Locate and identify every blood parasite.
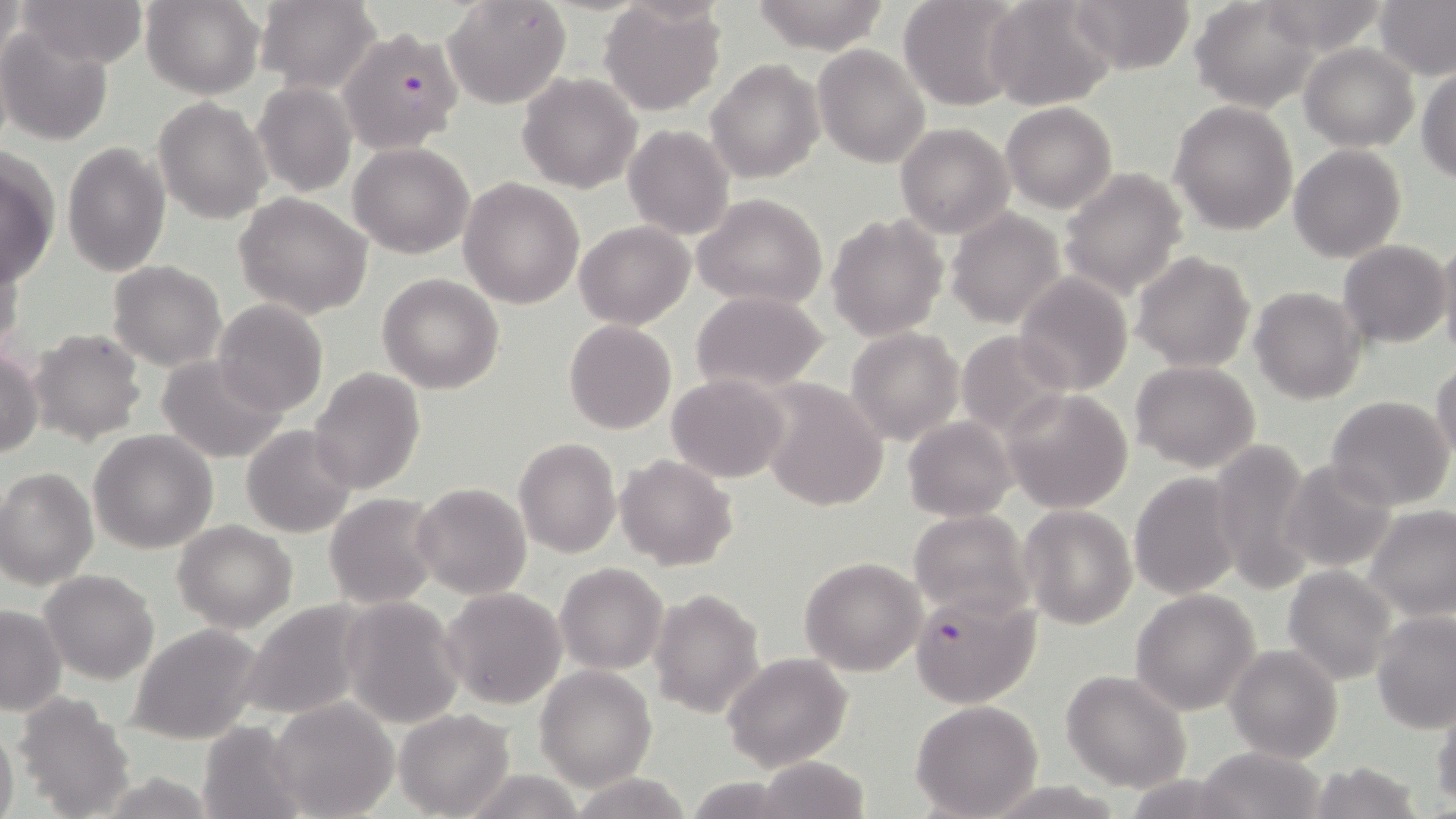

Approximate bounding boxes as (x1, y1, x2, y2) in pixels.
Plasmodium falciparum-infected red blood cells: (346, 25, 462, 150), (907, 589, 1042, 709).
No Plasmodium ovale, Plasmodium malariae, Plasmodium vivax, Babesia divergens, or Trypanosoma brucei observed.

Summary:
  - Uninfected red blood cell locations: (18, 0, 146, 67), (141, 0, 264, 98), (443, 0, 571, 111), (747, 0, 895, 53), (898, 0, 1026, 110), (983, 0, 1117, 111), (1069, 0, 1197, 75), (1190, 0, 1323, 112), (1375, 0, 1455, 81), (256, 1, 382, 93), (1257, 2, 1390, 54), (599, 3, 725, 115), (0, 24, 113, 147), (1299, 42, 1418, 150), (812, 44, 929, 170), (706, 58, 824, 184), (1417, 67, 1456, 183), (517, 73, 642, 193), (254, 81, 358, 196), (152, 97, 271, 223), (1168, 99, 1297, 235), (1001, 103, 1117, 214), (895, 122, 1014, 237), (624, 124, 735, 240), (61, 141, 171, 277), (348, 142, 473, 259), (1288, 145, 1406, 264), (1, 150, 61, 286), (1058, 168, 1189, 300), (458, 177, 584, 309), (693, 192, 827, 308), (235, 193, 372, 318), (945, 209, 1066, 328), (825, 212, 947, 343), (575, 220, 693, 329), (1436, 237, 1456, 360), (1339, 240, 1449, 348), (0, 245, 24, 364), (1131, 250, 1256, 372), (108, 259, 226, 371), (378, 273, 504, 394), (1013, 273, 1133, 395), (1248, 286, 1365, 405), (690, 289, 831, 393), (211, 299, 328, 417), (565, 319, 676, 434), (29, 328, 146, 445), (846, 328, 963, 444), (955, 331, 1070, 438), (0, 346, 43, 458), (156, 356, 287, 464), (1130, 360, 1260, 472), (1431, 361, 1456, 466), (309, 367, 426, 496), (667, 374, 789, 483), (760, 380, 889, 513), (1003, 389, 1133, 513), (1326, 395, 1455, 510), (903, 415, 1017, 521), (242, 424, 359, 538), (89, 430, 219, 553), (514, 436, 621, 559), (1206, 437, 1315, 596), (617, 455, 738, 570), (1281, 459, 1400, 573), (0, 466, 99, 589), (1128, 473, 1241, 601), (413, 482, 530, 600), (324, 493, 442, 608), (1018, 504, 1138, 629), (1366, 505, 1456, 620), (908, 510, 1032, 621), (173, 521, 297, 632), (799, 557, 926, 675), (555, 562, 667, 674), (1282, 565, 1396, 684), (41, 568, 159, 683), (441, 587, 568, 711), (649, 588, 764, 719), (1130, 589, 1261, 715), (339, 596, 465, 726), (240, 599, 375, 722), (0, 603, 66, 715), (1373, 613, 1456, 734), (1090, 615, 1253, 769), (128, 623, 266, 745), (1225, 644, 1343, 765), (723, 652, 854, 772), (535, 665, 656, 789), (1062, 670, 1191, 792), (11, 692, 137, 817), (1431, 695, 1456, 808), (268, 697, 398, 819), (911, 700, 1044, 818), (395, 709, 515, 817), (196, 719, 311, 819), (0, 725, 19, 819), (1195, 746, 1326, 819), (753, 757, 872, 818), (1304, 761, 1425, 819), (458, 767, 586, 819), (570, 773, 695, 817)
  - Slide-level diagnosis: Plasmodium falciparum
  - Magnification: 1000x
  - Modality: light microscopy
  - Field of view: one of a larger specimen
  - Image size: 1456×819 pixels
  - Preparation: thin blood film
  - Stain: May-Grünwald-Giemsa